Comment on the morphology of the red blood cells.
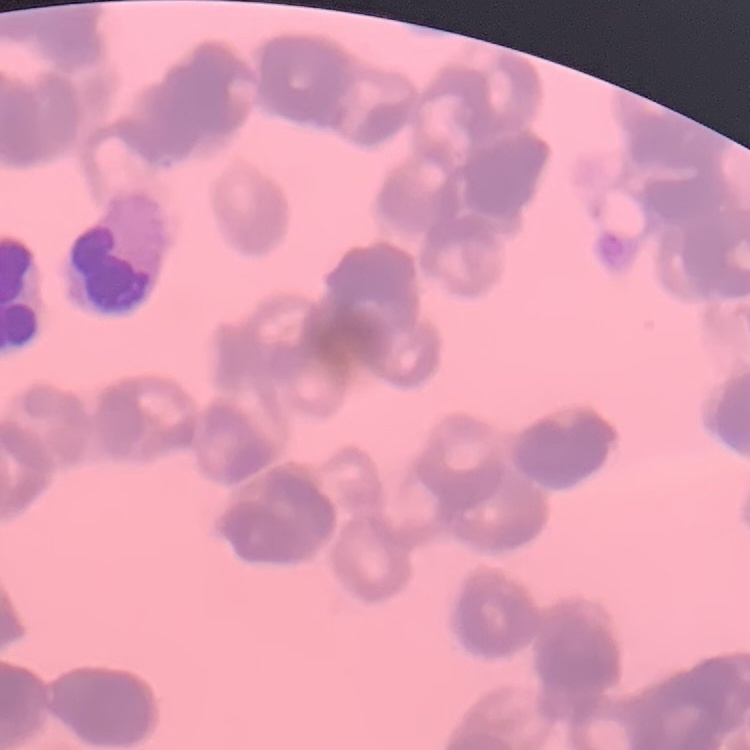

They show rouleaux formation.

Field's or Giemsa stain. Thin blood smear. Square crop of a larger photomicrograph.